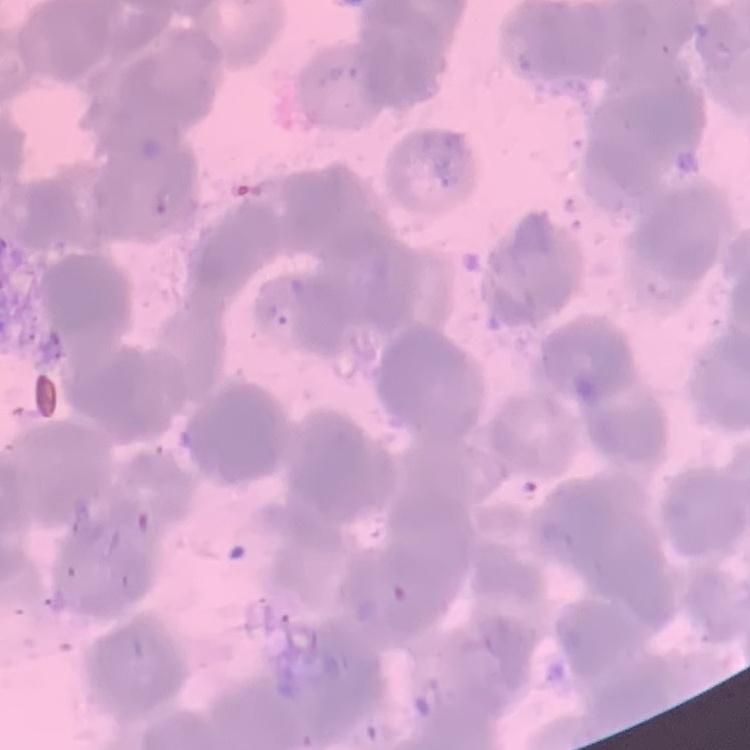
erythrocyte morphology = rouleaux formation
stain = Field's or Giemsa
preparation = thin blood film
image type = one tile cut from a larger photomicrograph